Report the malaria status of this cell.
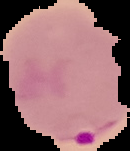
Parasitized.

Image is 130×151 pixels. From a thin blood film. The area outside the segmented cell region is set to black.